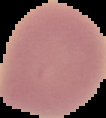 Cell region segmented out of the field of view; the surrounding area is masked to black. From a thin blood smear. Image is 106×118 pixels. Malaria status: uninfected.